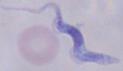
{
  "identification": "trypanosome",
  "modality": "photomicrograph",
  "magnification": "1000x"
}